Locate every Trypanosoma brucei.
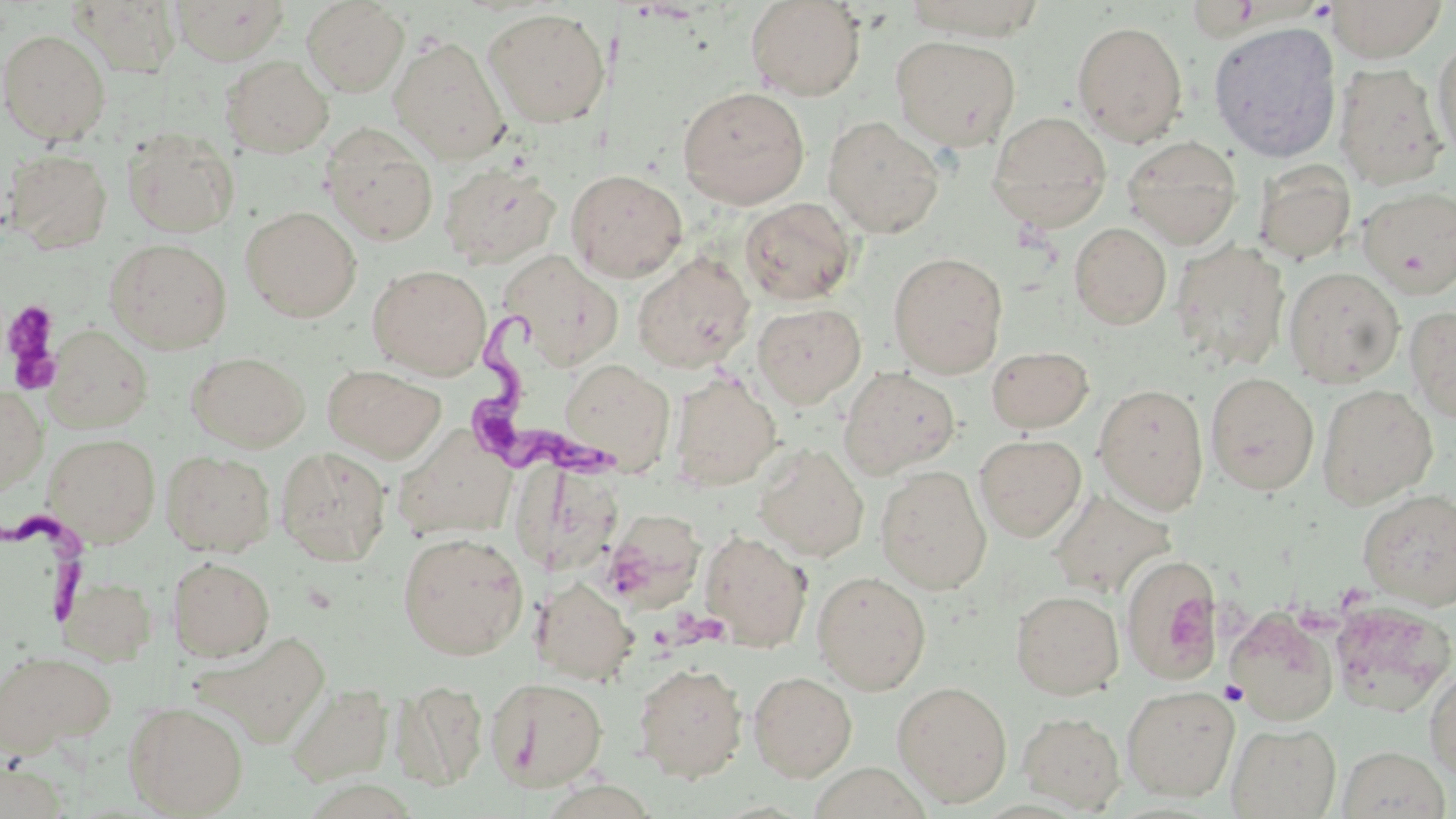
Approximate bounding boxes as (x1,y1)-(x2,y2) corner pairs in pixels.
Trypanosoma brucei: (460,313)-(627,489), (0,505)-(92,628).

{
  "slide_level_diagnosis": "Trypanosoma brucei",
  "modality": "optical microscopy",
  "stain": "May-Grünwald-Giemsa",
  "image_size": "1456×819 pixels",
  "preparation": "thin blood smear",
  "platelet_locations": "approximate bounding boxes as (x1,y1)-(x2,y2) corner pairs in pixels: (2,299)-(63,394), (1219,680)-(1247,704)",
  "uninfected_red_blood_cell_locations": "approximate bounding boxes as (x1,y1)-(x2,y2) corner pairs in pixels: (170,0)-(290,65), (745,0)-(866,101), (1327,0)-(1447,62), (69,1)-(182,77), (301,1)-(409,96), (902,1)-(1048,40), (483,8)-(610,127), (1071,20)-(1188,145), (1207,21)-(1342,163), (1,30)-(110,143), (389,35)-(510,164), (891,35)-(1021,151), (1432,35)-(1456,162), (221,55)-(333,158), (1334,62)-(1449,190), (677,87)-(810,209), (987,110)-(1112,232), (823,115)-(945,238), (320,124)-(438,246), (121,128)-(239,238), (1121,135)-(1243,248), (3,147)-(113,253), (439,162)-(561,268), (1254,162)-(1356,264), (566,169)-(688,282), (1357,187)-(1456,297), (739,197)-(858,305), (241,206)-(361,322), (1070,222)-(1171,329), (105,238)-(232,354), (1171,240)-(1289,371), (498,249)-(623,369), (888,251)-(1009,378), (632,252)-(756,373), (1174,252)-(1408,376), (367,264)-(491,378), (1283,267)-(1404,387), (752,302)-(866,408), (1405,305)-(1456,423), (44,325)-(153,432), (986,345)-(1094,433), (187,351)-(309,451), (559,359)-(675,474), (323,365)-(445,462), (838,366)-(960,479), (669,372)-(782,490), (1205,372)-(1319,495), (1094,384)-(1209,514), (1316,384)-(1438,508), (0,387)-(47,496), (394,424)-(519,533), (44,433)-(160,545), (974,434)-(1086,542), (753,443)-(869,561), (275,446)-(391,566), (161,450)-(276,557), (875,465)-(992,595), (517,468)-(625,576), (1358,488)-(1456,609), (1048,489)-(1174,599), (600,511)-(705,609), (700,529)-(813,651), (397,531)-(529,660), (1121,555)-(1222,681), (168,556)-(275,661), (812,570)-(931,695), (59,576)-(157,664), (533,578)-(638,685), (1011,589)-(1124,699), (1329,600)-(1455,717), (1225,606)-(1338,725), (194,631)-(331,748), (0,650)-(115,757), (632,661)-(749,782), (1424,665)-(1456,780), (748,671)-(857,781), (486,676)-(608,791), (392,680)-(489,789), (892,680)-(1012,806), (286,682)-(393,786), (1122,686)-(1239,801), (124,701)-(248,816), (1018,711)-(1126,812), (1227,723)-(1341,818), (1337,745)-(1450,818), (1,756)-(70,819)",
  "magnification": "1000x",
  "field_of_view": "single"
}